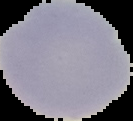
Summary:
  - Image type: cell region segmented out of the field of view; surrounding area masked to black
  - Image size: 133×121 pixels
  - Malaria status: uninfected
  - Preparation: thin blood film